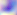
{
  "magnification": "400x",
  "identification": "Toxoplasma gondii",
  "modality": "photomicrograph"
}